Locate every malaria parasite.
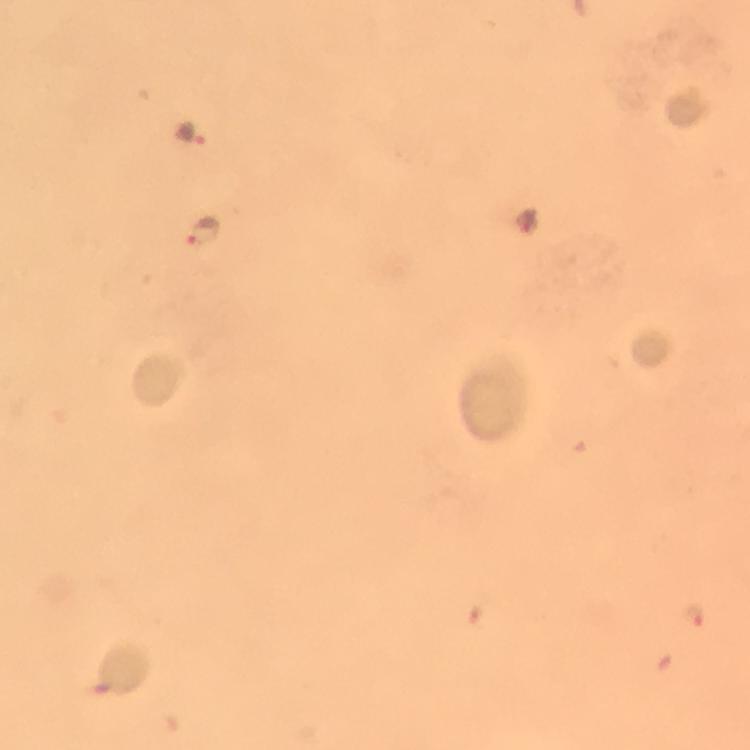
Approximate centers as (x, y) in pixels.
Malaria parasites: (188, 131), (201, 229), (699, 618).

Summary:
  - Context: from a malaria diagnostic workup
  - Preparation: thick blood film
  - Cropped from: a single field of view
  - Stain: Giemsa
  - Image size: 750×750 pixels
  - Capture: smartphone mounted on the microscope
  - Immersion oil: applied
  - Magnification: 100x